Classify this cell by malaria status.
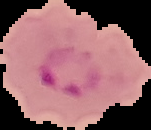
Parasitized.

Summary:
  - Image type: segmented cell region with the area outside set to black
  - Image size: 151×130 pixels
  - Preparation: thin blood film